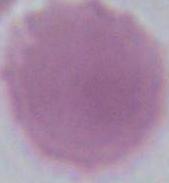
An erythrocyte is shown. Photomicrograph. 1000x magnification.